State which cell type is depicted.
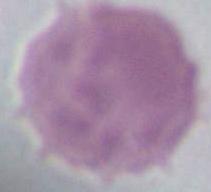

An erythrocyte.

magnification = 1000x
modality = micrograph